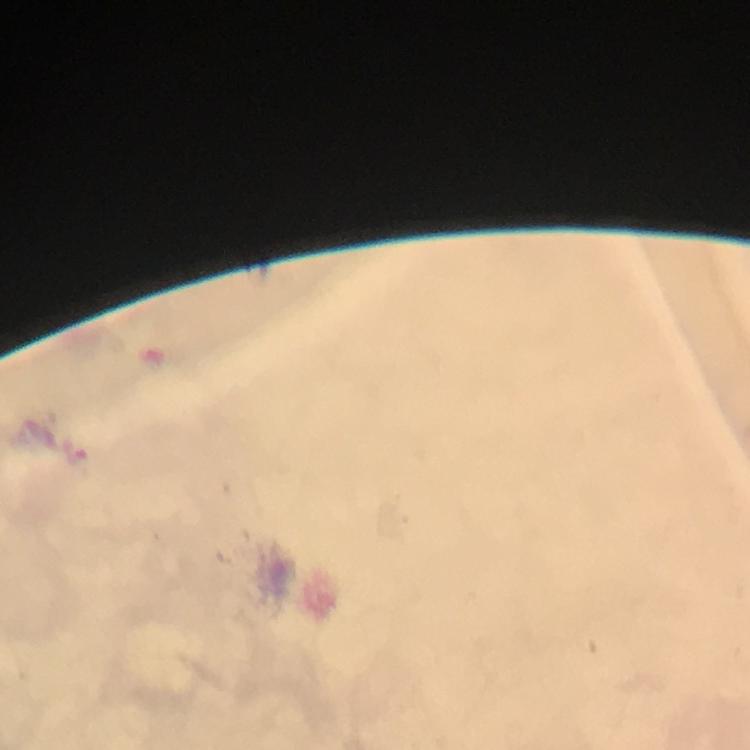

Approximate object centers, in pixels from the top-left corner. Malaria parasite locations: (x=78, y=454). Giemsa stain. Smartphone photograph taken through a microscope. From a diagnostic examination for malaria. Immersion oil applied. Cropped region of a single field of view. 100x magnification. Thick blood film. Image is 750×750 pixels.